Comment on the morphology of the erythrocytes.
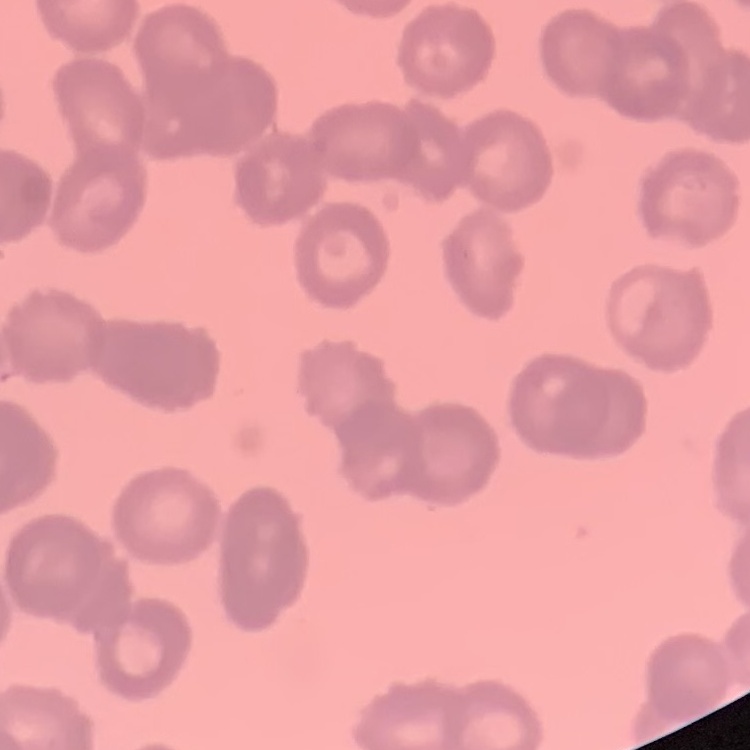

They show rouleaux formation.

Summary:
  - Preparation: thin blood film
  - Image type: one tile cut from a larger photomicrograph
  - Stain: Field's or Giemsa